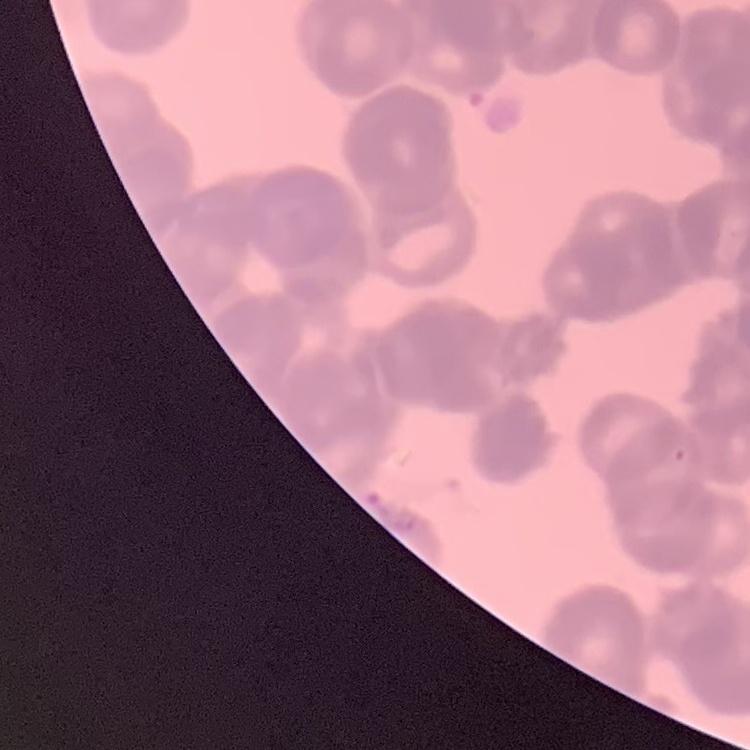
red blood cell morphology = rouleaux formation
preparation = thin blood smear
image type = one tile cut from a larger photomicrograph
stain = Field's or Giemsa